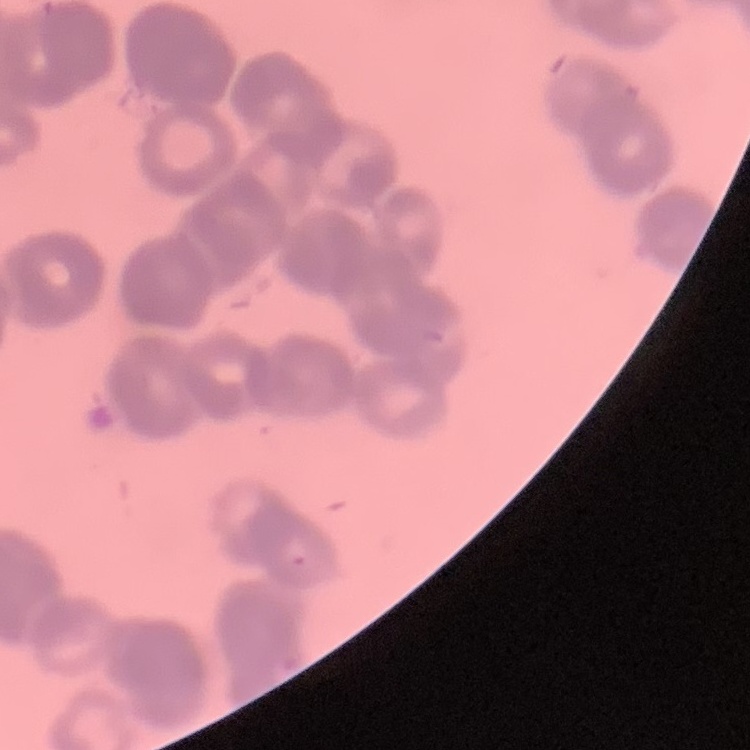

red blood cell morphology = rouleaux formation
preparation = thin peripheral smear
image type = square crop of a larger photomicrograph
stain = Field's or Giemsa